Report the malaria status of this cell.
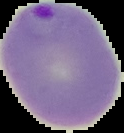
Parasitized.

Image is 124×133 pixels. From a thin blood smear. The area outside the segmented cell region is set to black.